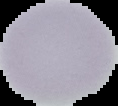

From a thin blood film. Malaria status: uninfected. Cell region segmented out of the field of view; the surrounding area is masked to black. Image is 118×106 pixels.